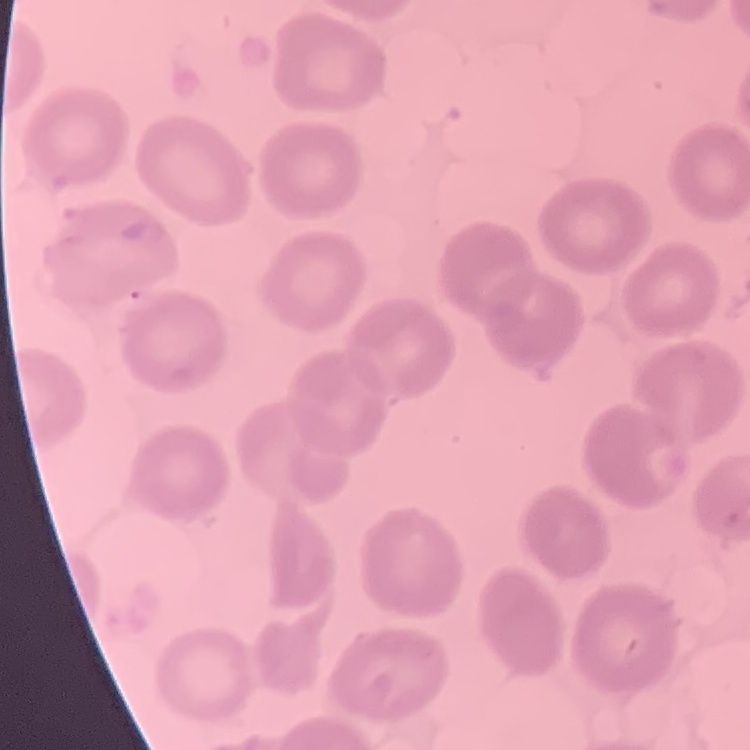
Summary:
  - Erythrocyte morphology: no rouleaux formation
  - Image type: square crop of a larger photomicrograph
  - Stain: Field's or Giemsa
  - Preparation: thin blood film